Give the position of every malaria parasite.
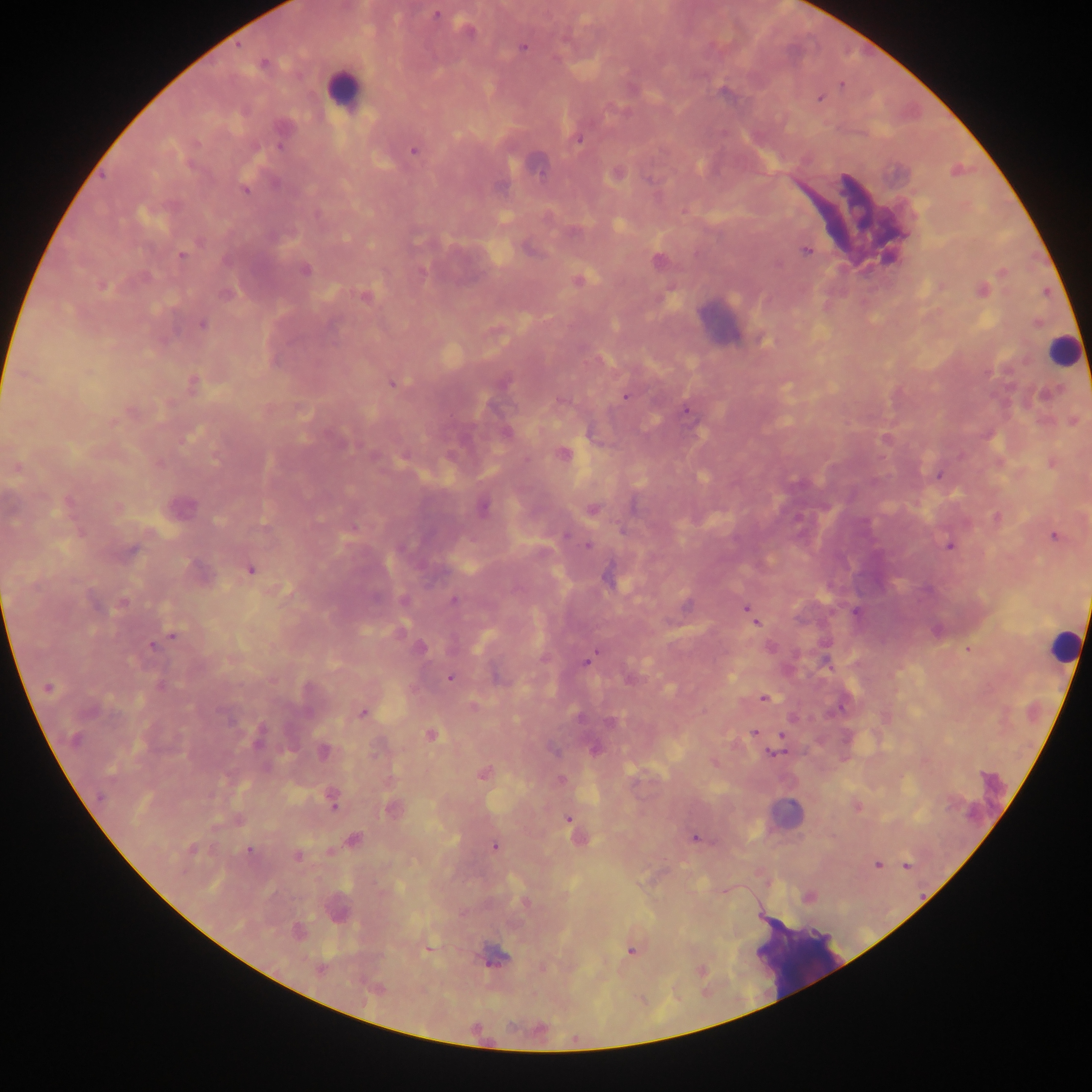
Approximate centers as [x, y] in pixels.
Malaria parasites: [436, 15], [468, 31], [523, 48], [263, 64], [842, 84], [820, 98], [578, 140], [413, 151], [245, 190], [200, 242], [806, 250], [180, 255], [305, 271], [577, 281], [103, 285], [982, 291], [226, 294], [365, 296], [202, 324], [193, 383], [393, 383], [1048, 394], [626, 396], [686, 411], [506, 432], [885, 438], [563, 454], [16, 468], [938, 475], [180, 506], [118, 507], [483, 508], [593, 510], [997, 518], [565, 536], [1054, 536], [588, 545], [949, 546], [131, 551], [251, 570], [607, 579], [404, 600], [453, 600], [123, 604], [687, 605], [747, 609], [855, 612], [753, 619], [174, 635], [152, 645], [421, 648], [968, 650], [825, 661], [586, 662], [450, 678], [160, 687], [47, 688], [764, 698], [474, 706], [362, 713], [579, 717], [611, 722], [753, 732], [782, 735], [431, 736], [258, 738], [74, 740], [595, 749], [324, 752], [773, 753], [484, 773], [101, 797], [333, 804], [391, 808], [568, 819], [354, 838], [694, 838], [495, 847], [191, 850], [249, 850], [298, 856], [877, 864], [906, 865], [809, 897], [525, 903], [632, 950], [494, 957], [320, 969], [701, 970].

Leukocyte locations: [342, 89], [720, 320], [1062, 350], [1063, 646], [802, 955]. Image is 1092×1092 pixels. Single field of view. Collected in Ghana. Thick blood film. Photographed through a microscope with a mobile-phone camera.